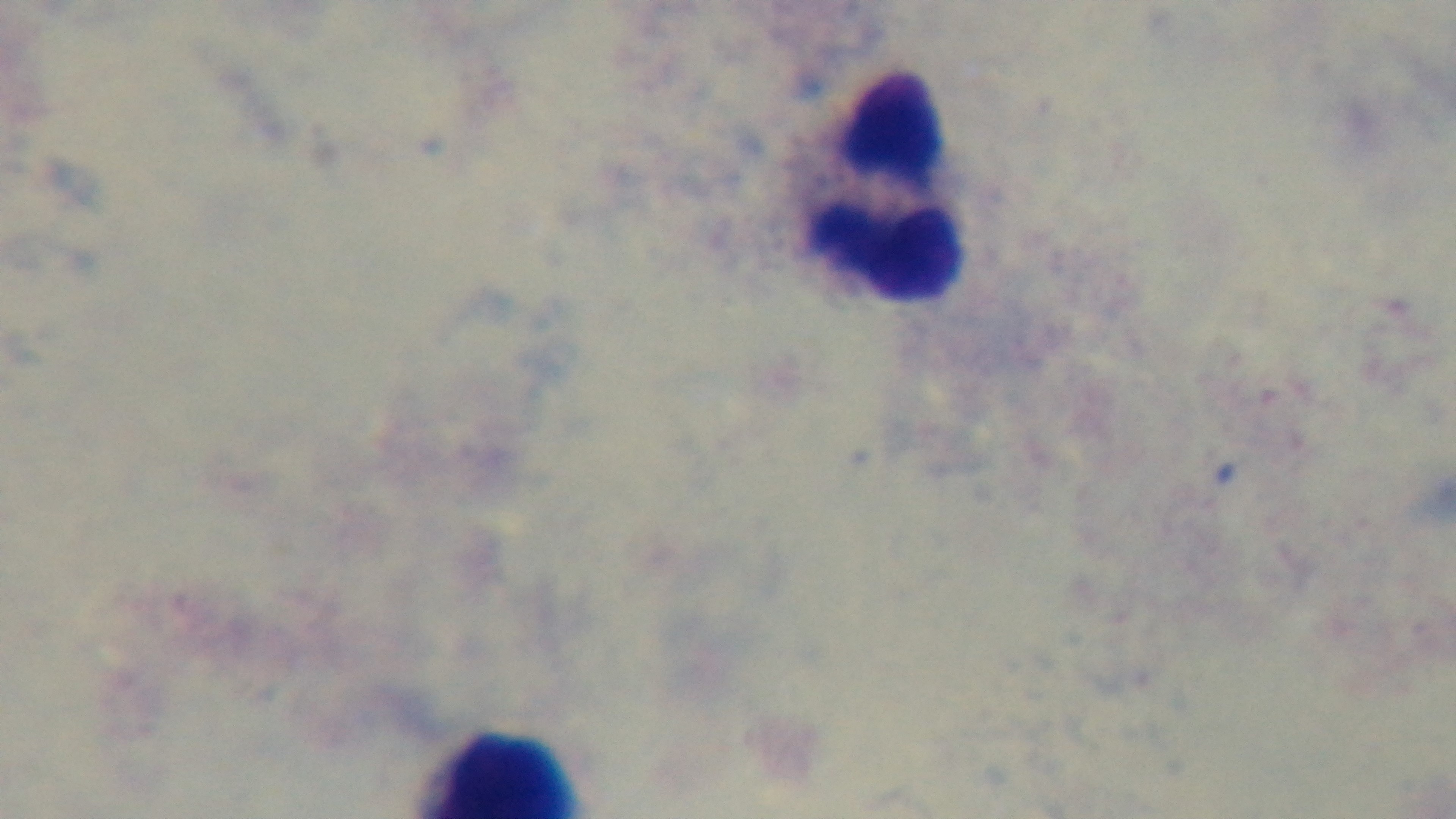

One field from the slide. Captured with a mounted 4K digital camera. Photomicrograph. 100x oil-immersion objective. Preparation: thick. Malaria status: uninfected. Giemsa-stained.